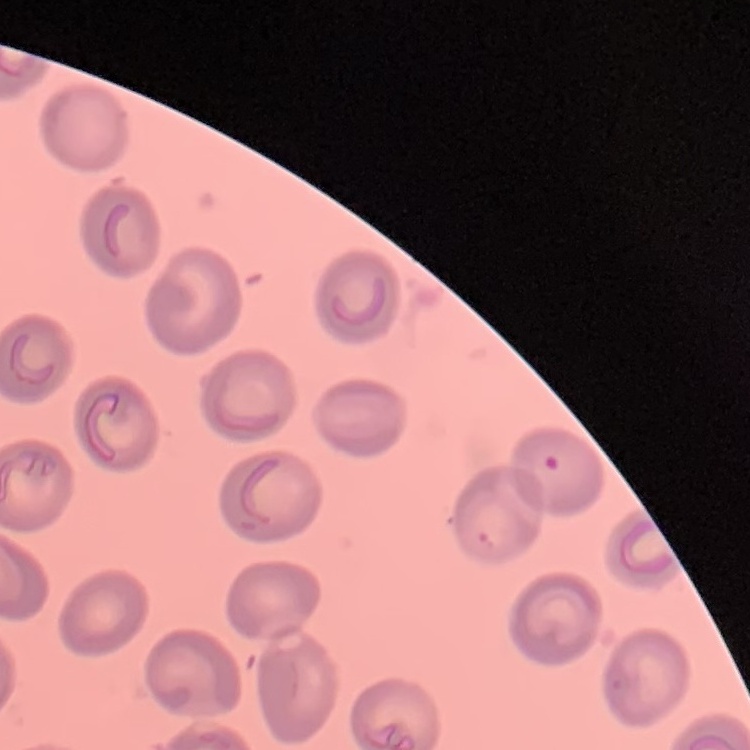 The red blood cells exhibit no rouleaux formation. Stained with either Field's or Giemsa. Square crop of a larger photomicrograph. Thin blood film.